Report the malaria status of this cell.
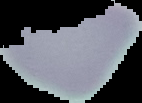

Uninfected.

preparation = thin blood film
image type = segmented cell region with the area outside set to black
image size = 142×103 pixels